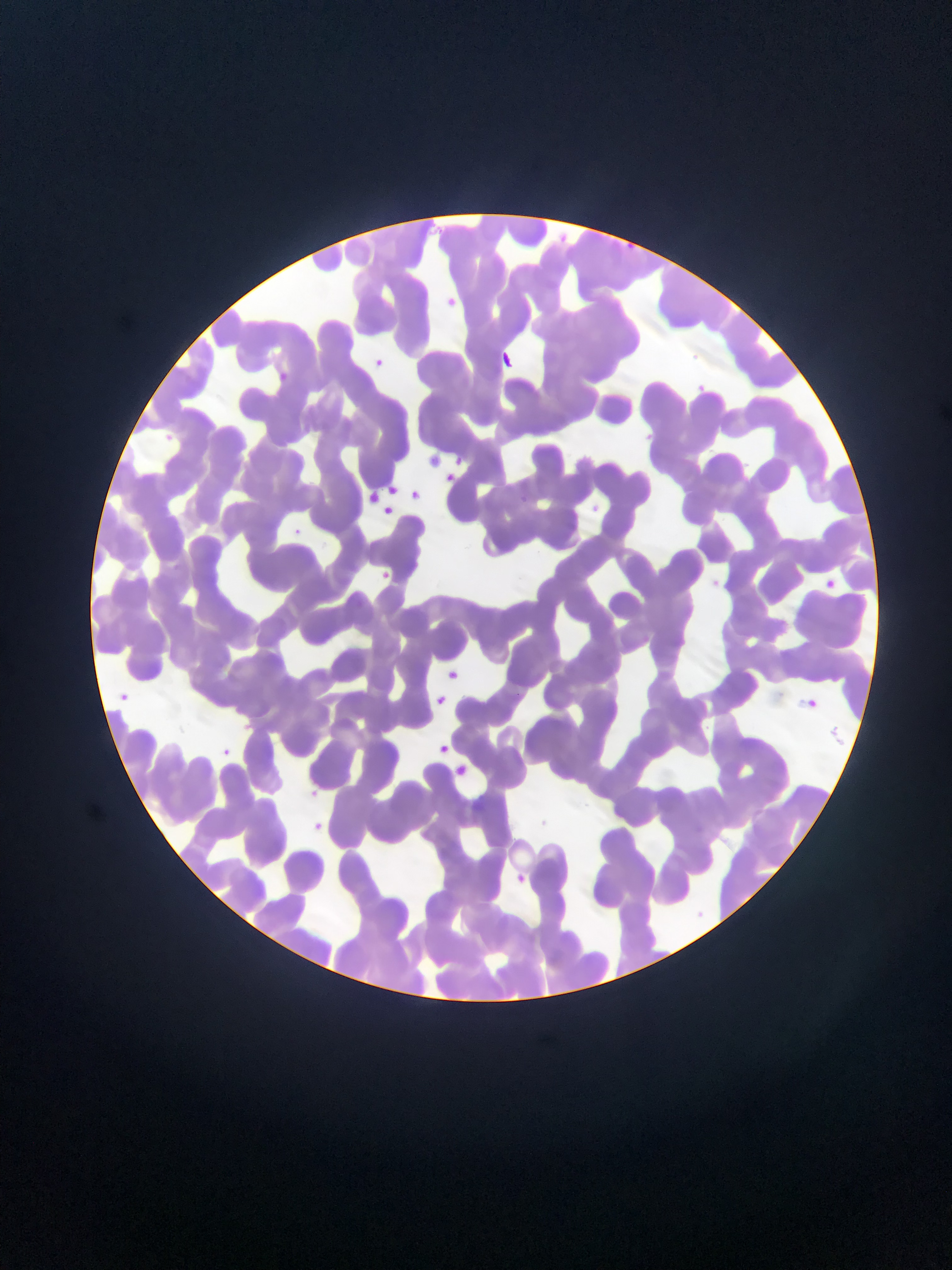
Approximate bounding boxes as (left, top, right, bottom) in pixels. Malaria parasite locations: (446, 289, 473, 315), (498, 346, 518, 362), (373, 351, 389, 368), (690, 379, 712, 399), (159, 430, 177, 446), (426, 446, 446, 467), (452, 448, 473, 467), (445, 469, 458, 483), (381, 470, 399, 493), (405, 487, 425, 505), (364, 489, 381, 507), (388, 500, 395, 518), (289, 525, 305, 539), (374, 569, 395, 587), (819, 575, 840, 594), (442, 665, 463, 685), (114, 688, 133, 705), (429, 691, 450, 711), (799, 696, 820, 715), (435, 742, 452, 758), (217, 745, 234, 761), (451, 762, 469, 778), (302, 786, 321, 803), (307, 817, 330, 839), (510, 870, 530, 889). One field of view. Sample from Ghana. Photographed through a microscope with a mobile-phone camera. Thin blood smear. Image is 952×1270 pixels.